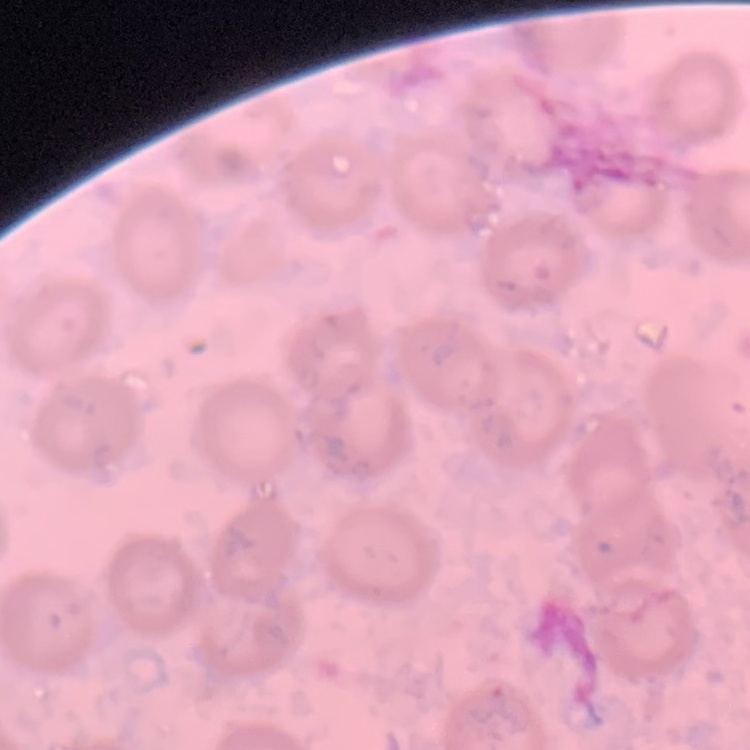 The erythrocytes exhibit no rouleaux formation. Thin peripheral smear. One tile cut from a larger photomicrograph. Field's or Giemsa stain.